Classify this cell by malaria status.
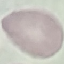
It is uninfected.

Summary:
  - Stain: Giemsa
  - Image type: automatically extracted cell patch, resized to 64 × 64 pixels
  - Preparation: thin blood smear
  - Capture: smartphone camera at the microscope eyepiece